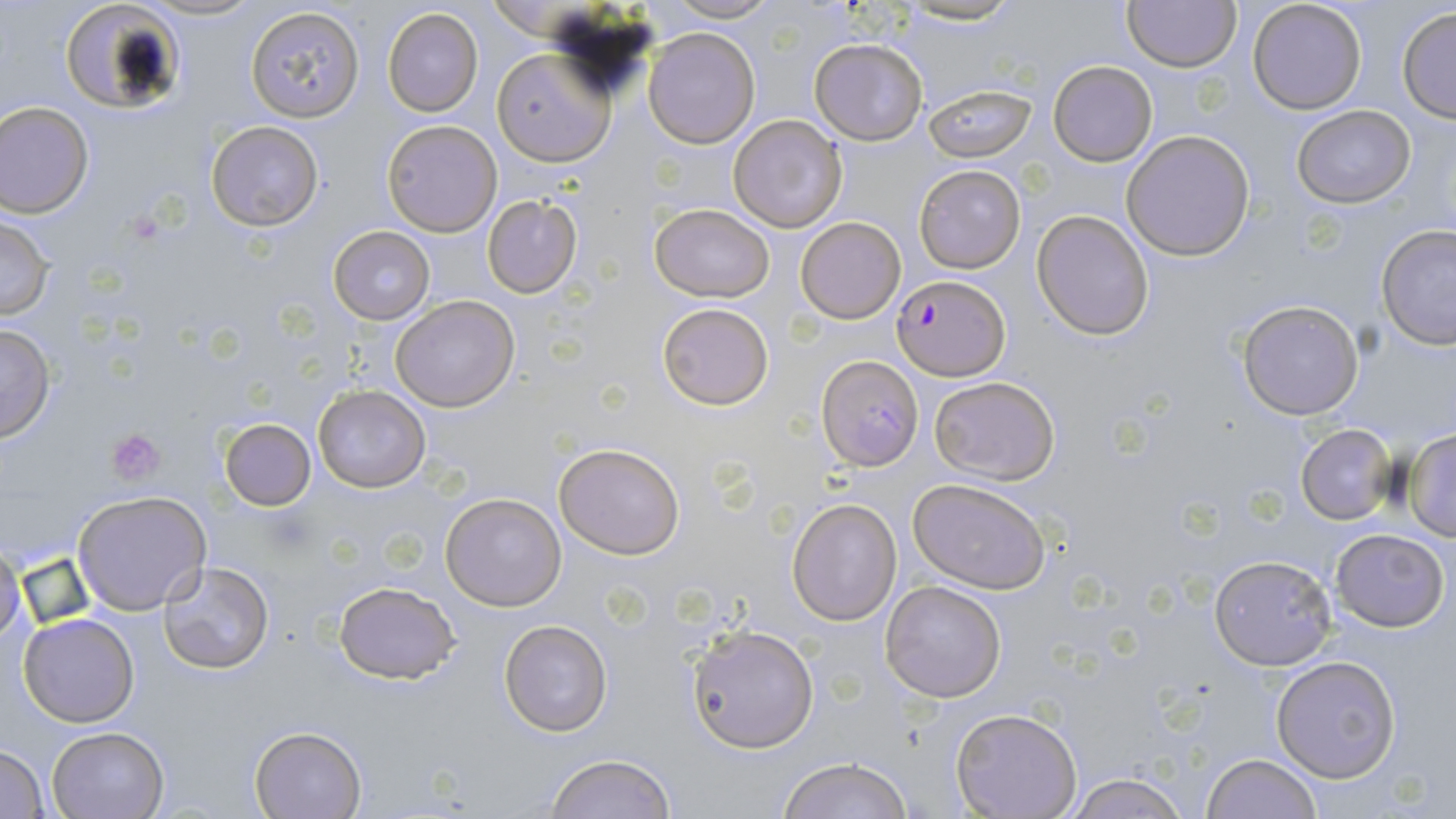 Approximate bounding boxes as named x1/y1/x2/y2 corners in pixels. Plasmodium falciparum-infected red blood cell locations: (x1=893, y1=274, x2=1009, y2=378), (x1=814, y1=357, x2=923, y2=472). Platelet locations: (x1=106, y1=428, x2=167, y2=486). Uninfected red blood cell locations: (x1=138, y1=0, x2=265, y2=22), (x1=655, y1=0, x2=786, y2=25), (x1=898, y1=0, x2=1024, y2=26), (x1=1122, y1=0, x2=1240, y2=72), (x1=1246, y1=0, x2=1368, y2=115), (x1=58, y1=2, x2=187, y2=115), (x1=245, y1=6, x2=365, y2=122), (x1=382, y1=7, x2=484, y2=117), (x1=1397, y1=7, x2=1456, y2=123), (x1=642, y1=26, x2=760, y2=148), (x1=809, y1=37, x2=927, y2=146), (x1=492, y1=48, x2=614, y2=166), (x1=1049, y1=61, x2=1157, y2=166), (x1=922, y1=82, x2=1036, y2=161), (x1=0, y1=100, x2=95, y2=218), (x1=1290, y1=104, x2=1416, y2=208), (x1=728, y1=113, x2=849, y2=234), (x1=382, y1=120, x2=501, y2=236), (x1=206, y1=121, x2=324, y2=231), (x1=1121, y1=130, x2=1256, y2=261), (x1=914, y1=164, x2=1026, y2=273), (x1=482, y1=195, x2=583, y2=297), (x1=650, y1=203, x2=775, y2=302), (x1=1032, y1=209, x2=1155, y2=340), (x1=0, y1=212, x2=57, y2=321), (x1=795, y1=216, x2=906, y2=324), (x1=330, y1=225, x2=435, y2=325), (x1=1376, y1=225, x2=1456, y2=349), (x1=392, y1=295, x2=519, y2=412), (x1=1236, y1=298, x2=1365, y2=420), (x1=656, y1=302, x2=774, y2=411), (x1=0, y1=322, x2=56, y2=444), (x1=928, y1=376, x2=1060, y2=485), (x1=313, y1=385, x2=430, y2=492), (x1=220, y1=418, x2=316, y2=510), (x1=1295, y1=423, x2=1399, y2=526), (x1=1402, y1=428, x2=1456, y2=540), (x1=554, y1=442, x2=684, y2=559), (x1=908, y1=478, x2=1051, y2=594), (x1=72, y1=491, x2=212, y2=614), (x1=441, y1=492, x2=566, y2=610), (x1=786, y1=498, x2=902, y2=626), (x1=1329, y1=528, x2=1450, y2=632), (x1=0, y1=539, x2=27, y2=649), (x1=1209, y1=554, x2=1336, y2=669), (x1=158, y1=562, x2=273, y2=676), (x1=334, y1=579, x2=461, y2=685), (x1=879, y1=579, x2=1007, y2=703), (x1=18, y1=612, x2=140, y2=728), (x1=498, y1=620, x2=613, y2=736), (x1=686, y1=625, x2=819, y2=753), (x1=1270, y1=654, x2=1402, y2=784), (x1=951, y1=708, x2=1081, y2=818), (x1=250, y1=726, x2=366, y2=818), (x1=47, y1=727, x2=168, y2=818), (x1=0, y1=744, x2=50, y2=818), (x1=1199, y1=752, x2=1323, y2=819), (x1=542, y1=753, x2=681, y2=819), (x1=776, y1=757, x2=916, y2=818), (x1=1059, y1=774, x2=1194, y2=818). Slide-level diagnosis: Plasmodium falciparum. Thin blood smear. Image is 1456×819 pixels. Optical microscopy. May-Grünwald-Giemsa-stained preparation. Captured at 1000x magnification. Single field of view.